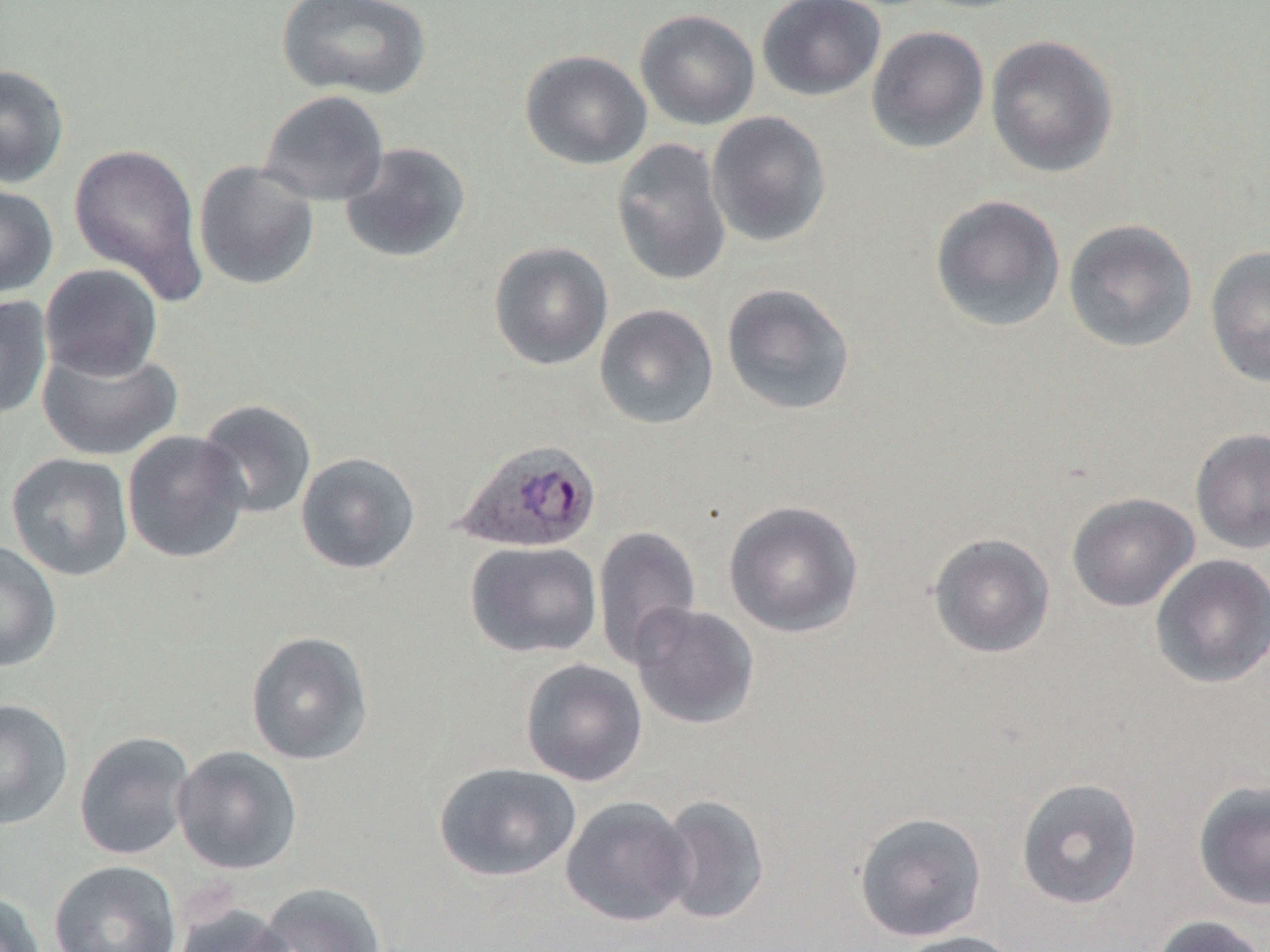

Approximate bounding boxes as (x1,y1)-(x2,y2) corner pairs in pixels. Uninfected red blood cell locations: (276,0)-(432,100), (757,0)-(886,101), (635,9)-(760,130), (865,25)-(990,154), (985,34)-(1119,178), (520,49)-(652,170), (0,63)-(69,188), (258,90)-(390,206), (706,111)-(832,248), (611,137)-(732,287), (339,142)-(472,264), (68,143)-(207,303), (193,160)-(320,290), (0,183)-(58,298), (929,194)-(1066,333), (1063,218)-(1198,353), (488,241)-(614,370), (1204,246)-(1270,388), (39,263)-(163,381), (721,282)-(856,417), (0,295)-(53,421), (594,303)-(719,430), (37,342)-(183,462), (195,399)-(318,520), (1190,428)-(1270,555), (122,429)-(251,564), (6,452)-(134,582), (295,452)-(421,575), (1067,492)-(1199,612), (723,499)-(865,638), (592,525)-(702,669), (927,533)-(1055,659), (0,539)-(62,672), (465,540)-(603,659), (1150,554)-(1270,690), (627,602)-(759,729), (245,630)-(374,765), (519,658)-(648,787), (0,698)-(74,830), (73,730)-(195,860), (171,745)-(303,876), (432,761)-(582,883), (1015,777)-(1143,910), (1192,779)-(1270,911), (654,794)-(770,925), (560,795)-(694,927), (854,811)-(988,942), (48,860)-(182,952), (253,883)-(387,952), (0,890)-(48,952), (171,902)-(297,952), (1148,914)-(1268,952), (890,930)-(1026,952). Plasmodium ovale-infected red blood cell locations: (451,437)-(602,554). Slide-level diagnosis: Plasmodium ovale. Image is 1270×952 pixels. Thin blood smear. Optical microscopy. One field of a larger specimen. Captured at 1000x magnification.